Name the blood parasite species.
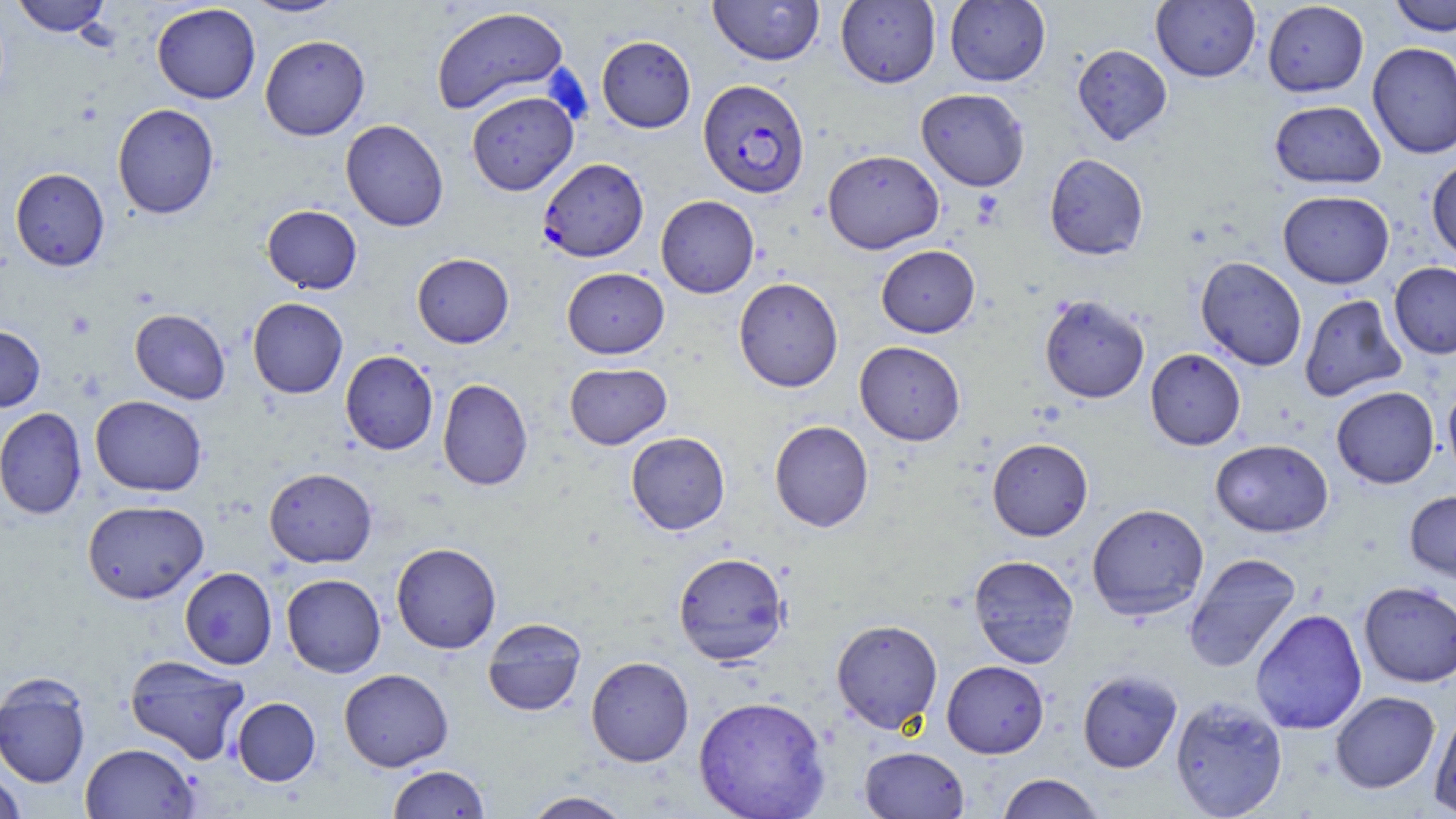
Plasmodium falciparum.

{
  "magnification": "1000x",
  "modality": "optical microscopy",
  "field_of_view": "single",
  "image_size": "1456×819 pixels",
  "plasmodium_falciparum_infected_red_blood_cell_locations": "approximate bounding boxes as named x1/y1/x2/y2 corners in pixels: (x1=698, y1=79, x2=810, y2=199), (x1=538, y1=158, x2=649, y2=262)",
  "stain": "May-Grünwald-Giemsa",
  "uninfected_red_blood_cell_locations": "approximate bounding boxes as named x1/y1/x2/y2 corners in pixels: (x1=12, y1=0, x2=111, y2=37), (x1=243, y1=0, x2=349, y2=18), (x1=708, y1=0, x2=825, y2=66), (x1=835, y1=0, x2=941, y2=88), (x1=945, y1=0, x2=1051, y2=86), (x1=1389, y1=0, x2=1455, y2=36), (x1=1150, y1=1, x2=1261, y2=82), (x1=1262, y1=1, x2=1369, y2=97), (x1=151, y1=3, x2=261, y2=104), (x1=430, y1=7, x2=569, y2=115), (x1=259, y1=34, x2=370, y2=140), (x1=597, y1=35, x2=696, y2=132), (x1=1367, y1=41, x2=1456, y2=159), (x1=1072, y1=44, x2=1172, y2=146), (x1=916, y1=88, x2=1030, y2=191), (x1=466, y1=90, x2=578, y2=196), (x1=1269, y1=100, x2=1386, y2=189), (x1=112, y1=102, x2=220, y2=220), (x1=340, y1=119, x2=449, y2=232), (x1=823, y1=149, x2=944, y2=254), (x1=1044, y1=153, x2=1149, y2=260), (x1=1426, y1=157, x2=1456, y2=261), (x1=10, y1=167, x2=110, y2=271), (x1=1278, y1=190, x2=1394, y2=288), (x1=655, y1=195, x2=759, y2=298), (x1=262, y1=205, x2=362, y2=294), (x1=876, y1=245, x2=980, y2=338), (x1=412, y1=253, x2=514, y2=348), (x1=1195, y1=256, x2=1307, y2=371), (x1=1389, y1=261, x2=1456, y2=359), (x1=562, y1=268, x2=669, y2=358), (x1=734, y1=277, x2=843, y2=392), (x1=1299, y1=294, x2=1406, y2=402), (x1=1039, y1=295, x2=1150, y2=403), (x1=247, y1=297, x2=348, y2=398), (x1=130, y1=309, x2=230, y2=404), (x1=0, y1=325, x2=45, y2=412), (x1=854, y1=341, x2=966, y2=445), (x1=1145, y1=348, x2=1246, y2=450), (x1=340, y1=350, x2=438, y2=455), (x1=564, y1=362, x2=672, y2=449), (x1=438, y1=378, x2=533, y2=491), (x1=1443, y1=380, x2=1456, y2=484), (x1=1331, y1=386, x2=1439, y2=489), (x1=90, y1=395, x2=207, y2=496), (x1=0, y1=407, x2=87, y2=520), (x1=769, y1=420, x2=874, y2=532), (x1=625, y1=431, x2=730, y2=535), (x1=987, y1=438, x2=1093, y2=541), (x1=1210, y1=439, x2=1333, y2=537), (x1=264, y1=468, x2=378, y2=568), (x1=1405, y1=490, x2=1456, y2=581), (x1=82, y1=500, x2=209, y2=604), (x1=1086, y1=503, x2=1209, y2=621), (x1=391, y1=542, x2=502, y2=653), (x1=673, y1=551, x2=789, y2=666), (x1=1183, y1=553, x2=1302, y2=672), (x1=968, y1=555, x2=1079, y2=668), (x1=179, y1=567, x2=277, y2=669), (x1=281, y1=573, x2=386, y2=677), (x1=1358, y1=581, x2=1456, y2=687), (x1=1250, y1=608, x2=1367, y2=735), (x1=482, y1=617, x2=587, y2=717), (x1=831, y1=618, x2=943, y2=734), (x1=125, y1=655, x2=250, y2=764), (x1=585, y1=656, x2=694, y2=766), (x1=942, y1=660, x2=1049, y2=758), (x1=339, y1=668, x2=453, y2=771), (x1=1077, y1=670, x2=1182, y2=773), (x1=0, y1=675, x2=91, y2=789), (x1=1330, y1=691, x2=1440, y2=794), (x1=693, y1=695, x2=831, y2=819), (x1=231, y1=697, x2=321, y2=786), (x1=1170, y1=697, x2=1288, y2=818), (x1=1429, y1=706, x2=1456, y2=815), (x1=80, y1=742, x2=199, y2=818), (x1=859, y1=746, x2=969, y2=818), (x1=387, y1=764, x2=490, y2=818), (x1=0, y1=769, x2=26, y2=818), (x1=996, y1=773, x2=1105, y2=818), (x1=522, y1=790, x2=635, y2=819)",
  "preparation": "thin blood film",
  "platelet_locations": "approximate bounding boxes as named x1/y1/x2/y2 corners in pixels: (x1=970, y1=190, x2=1005, y2=228)"
}